Assess this cell for malaria.
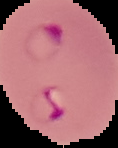
Parasitized.

Summary:
  - Image size: 118×148 pixels
  - Image type: cell region segmented out of the field of view; surrounding area masked to black
  - Preparation: thin blood film